Name the cell type shown.
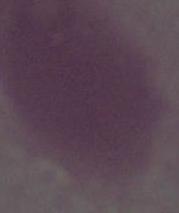
An erythrocyte.

magnification = 1000x
modality = micrograph